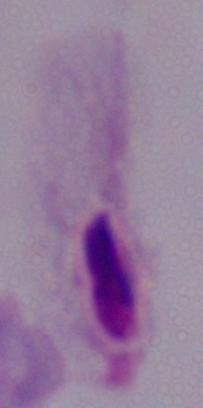
Summary:
  - Modality: micrograph
  - Identification: trichomonad
  - Magnification: 1000x